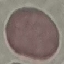
malaria status = uninfected
image type = cell patch, automatically extracted from a larger field of view and resized to 64 × 64 pixels
capture = smartphone camera at the microscope eyepiece
stain = Giemsa
preparation = thin smear